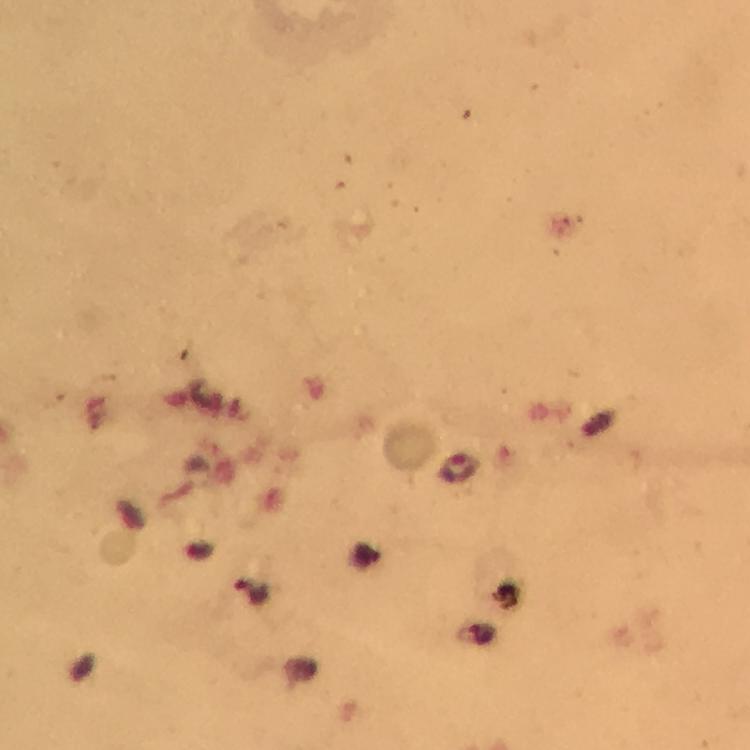

{
  "context": "from a malaria diagnostic workup",
  "plasmodium_parasite_locations": "approximate object centers, in pixels from the top-left corner: (x=459, y=469), (x=251, y=592)",
  "immersion_oil": "used",
  "capture": "smartphone mounted on the microscope",
  "image_size": "750×750 pixels",
  "magnification": "100x",
  "preparation": "thick blood film",
  "cropped_from": "one field of view",
  "stain": "Giemsa"
}